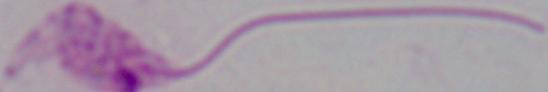
Captured at 1000x magnification. A Leishmania parasite is seen. Micrograph.